Identify the cell.
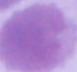

This is an erythrocyte.

Captured at 1000x magnification. Photomicrograph.